State the blood parasite species.
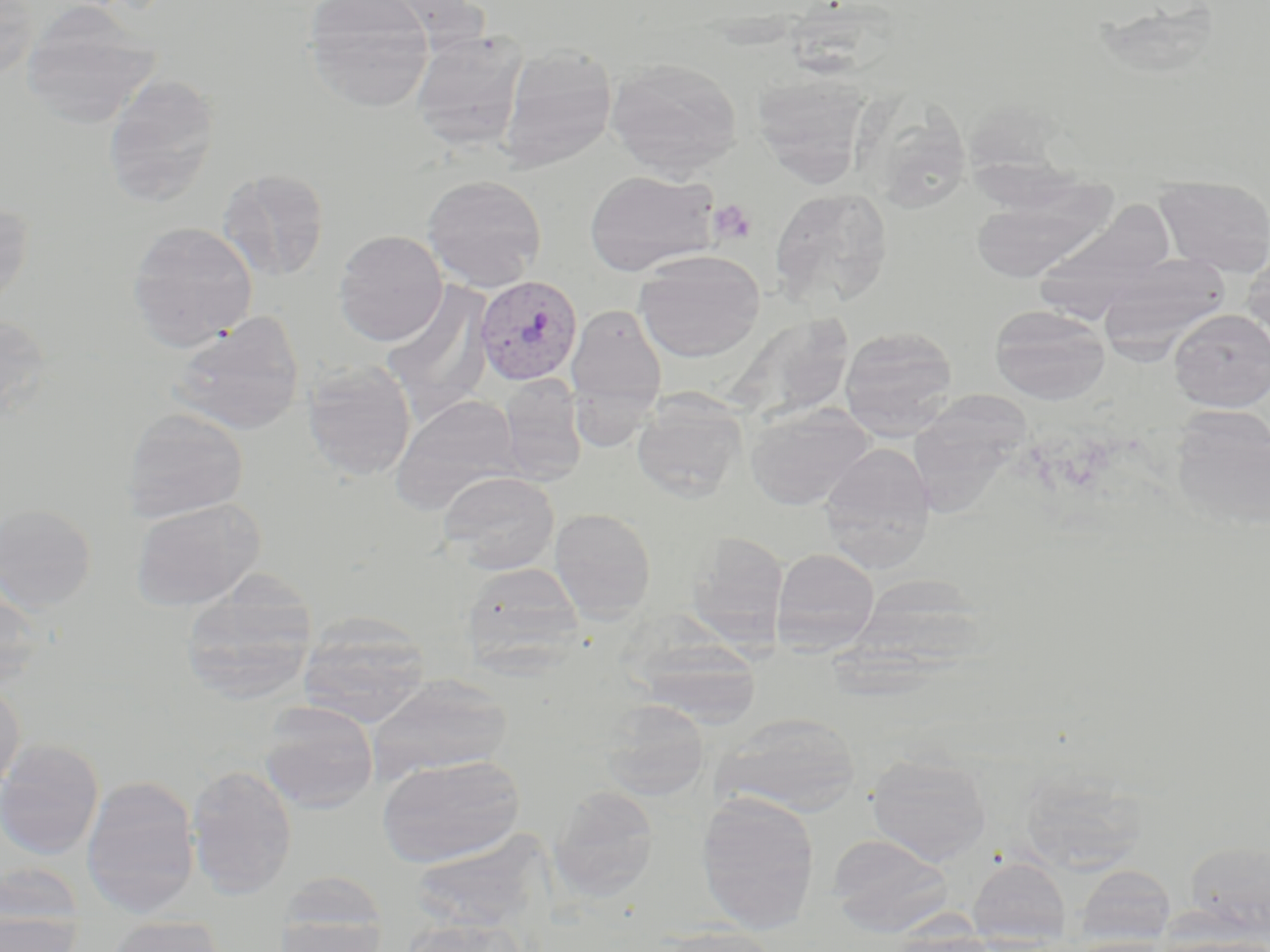
Plasmodium vivax.

Summary:
  - Coordinate format: approximate bounding boxes as [x1, y1, x2, y2] in pixels
  - Uninfected red blood cell locations: [302, 0, 434, 111], [0, 1, 38, 82], [20, 4, 160, 129], [410, 30, 530, 153], [498, 44, 618, 173], [605, 57, 742, 179], [751, 71, 873, 185], [102, 72, 221, 207], [217, 168, 330, 282], [584, 169, 718, 276], [422, 173, 548, 290], [969, 175, 1117, 282], [1155, 175, 1270, 277], [768, 187, 894, 310], [0, 200, 34, 310], [1031, 203, 1177, 317], [127, 220, 259, 352], [333, 230, 448, 346], [1242, 248, 1270, 354], [634, 251, 765, 362], [1097, 255, 1232, 359], [381, 282, 495, 417], [566, 303, 668, 415], [990, 305, 1110, 405], [1169, 309, 1270, 411], [169, 310, 307, 435], [727, 312, 855, 425], [0, 314, 53, 421], [839, 325, 958, 438], [301, 360, 417, 481], [500, 375, 587, 485], [910, 375, 1031, 516], [390, 393, 523, 513], [631, 393, 746, 502], [744, 402, 875, 510], [121, 407, 249, 523], [1169, 407, 1269, 532], [819, 442, 937, 570], [439, 471, 559, 575], [129, 497, 265, 610], [0, 503, 97, 612], [549, 507, 657, 621], [687, 531, 788, 644], [771, 547, 880, 654], [459, 561, 586, 672], [178, 580, 318, 704], [0, 589, 47, 694], [297, 613, 432, 727], [630, 636, 764, 726], [367, 674, 513, 782], [0, 679, 25, 798], [599, 700, 710, 802], [258, 701, 379, 814], [713, 712, 862, 816], [0, 738, 104, 860], [377, 754, 526, 867], [866, 754, 992, 865], [185, 765, 297, 899], [1019, 769, 1150, 874], [81, 774, 200, 917], [549, 786, 660, 903], [696, 792, 820, 935], [828, 833, 951, 934], [1185, 839, 1270, 942], [968, 855, 1071, 948], [0, 861, 84, 945], [1076, 864, 1176, 946], [272, 888, 389, 952], [0, 915, 83, 951], [105, 915, 228, 952], [402, 917, 530, 952], [648, 925, 781, 952], [884, 932, 1005, 952], [1155, 934, 1270, 952]
  - Platelet locations: [708, 199, 757, 245]
  - Plasmodium vivax-infected red blood cell locations: [474, 275, 582, 385]
  - Image size: 1270×952 pixels
  - Preparation: thin blood film
  - Field of view: one of a larger specimen
  - Stain: May-Grünwald-Giemsa
  - Magnification: 1000x
  - Modality: optical microscopy